Outline each blood parasite and name the species.
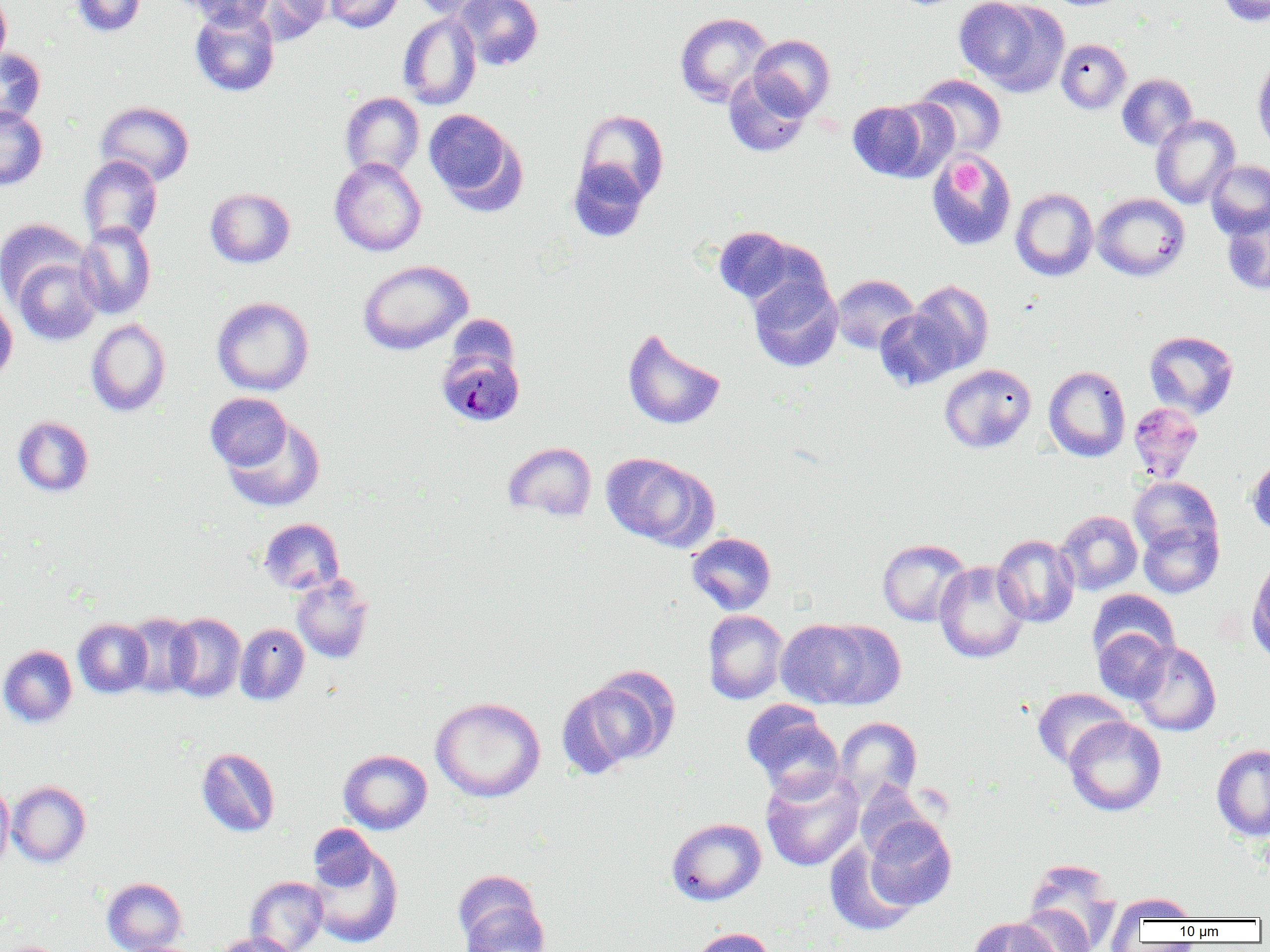

Approximate bounding boxes as (x1,y1)-(x2,y2) corner pairs in pixels.
Plasmodium malariae-infected red blood cells: (439,342)-(526,421).
No Plasmodium falciparum, Plasmodium ovale, Plasmodium vivax, Babesia divergens, or Trypanosoma brucei observed.

slide-level diagnosis = Plasmodium malariae
field of view = single
image size = 1270×952 pixels
uninfected red blood cell locations = approximate bounding boxes as (x1,y1)-(x2,y2) corner pairs in pixels: (70,0)-(147,37), (180,0)-(275,29), (250,0)-(332,44), (324,0)-(404,33), (408,0)-(500,20), (454,0)-(544,71), (954,0)-(1067,94), (1215,0)-(1270,25), (0,1)-(11,71), (189,4)-(280,97), (398,12)-(482,110), (674,12)-(774,107), (694,15)-(813,138), (749,35)-(835,119), (1056,39)-(1131,113), (0,48)-(45,127), (1252,55)-(1270,153), (723,73)-(811,157), (912,73)-(1007,160), (1117,74)-(1197,151), (340,92)-(424,179), (846,99)-(943,182), (95,101)-(195,186), (0,105)-(48,190), (424,109)-(525,213), (576,109)-(669,205), (1151,115)-(1240,209), (927,154)-(1016,251), (78,155)-(162,245), (330,157)-(426,256), (568,160)-(649,242), (1206,160)-(1270,238), (205,187)-(295,267), (1010,188)-(1098,281), (1092,193)-(1190,281), (1222,210)-(1270,295), (0,218)-(89,305), (75,220)-(156,319), (712,226)-(803,307), (13,256)-(102,346), (358,260)-(473,354), (748,274)-(843,372), (831,274)-(919,354), (907,280)-(994,375), (0,296)-(17,386), (212,296)-(314,396), (875,307)-(961,391), (86,319)-(171,416), (622,328)-(726,430), (1144,330)-(1238,419), (939,363)-(1036,453), (1043,365)-(1131,462), (205,392)-(293,472), (1127,402)-(1204,482), (222,415)-(325,512), (12,416)-(94,497), (503,442)-(597,522), (600,452)-(717,549), (1247,455)-(1270,537), (1129,476)-(1221,558), (1055,510)-(1142,596), (259,518)-(344,595), (1138,519)-(1223,598), (686,532)-(776,615), (992,534)-(1079,628), (877,538)-(971,626), (1247,554)-(1270,667), (934,561)-(1029,663), (291,574)-(374,663), (1087,589)-(1179,667), (702,610)-(788,704), (122,612)-(199,698), (165,612)-(246,702), (73,618)-(153,698), (775,618)-(887,710), (235,623)-(309,705), (1093,627)-(1174,704), (1130,641)-(1221,736), (0,645)-(77,727), (565,668)-(680,773), (1032,688)-(1130,769), (431,696)-(545,802), (741,700)-(843,798), (1064,716)-(1166,815), (834,717)-(922,806), (1211,743)-(1270,841), (197,747)-(280,836), (338,749)-(432,834), (760,768)-(864,871), (6,781)-(91,867), (853,781)-(936,860), (0,782)-(14,873), (864,817)-(956,911), (666,818)-(767,905), (308,824)-(378,891), (307,841)-(404,949), (824,841)-(918,936), (1023,857)-(1122,951), (453,872)-(549,952), (245,876)-(328,952), (102,877)-(186,952), (1107,892)-(1199,937), (1013,904)-(1095,952), (966,917)-(1064,952), (688,927)-(776,952), (213,933)-(297,952), (1,941)-(66,952)
preparation = thin blood smear
platelet locations = approximate bounding boxes as (x1,y1)-(x2,y2) corner pairs in pixels: (952,159)-(985,197)
magnification = 1000x
modality = optical microscopy